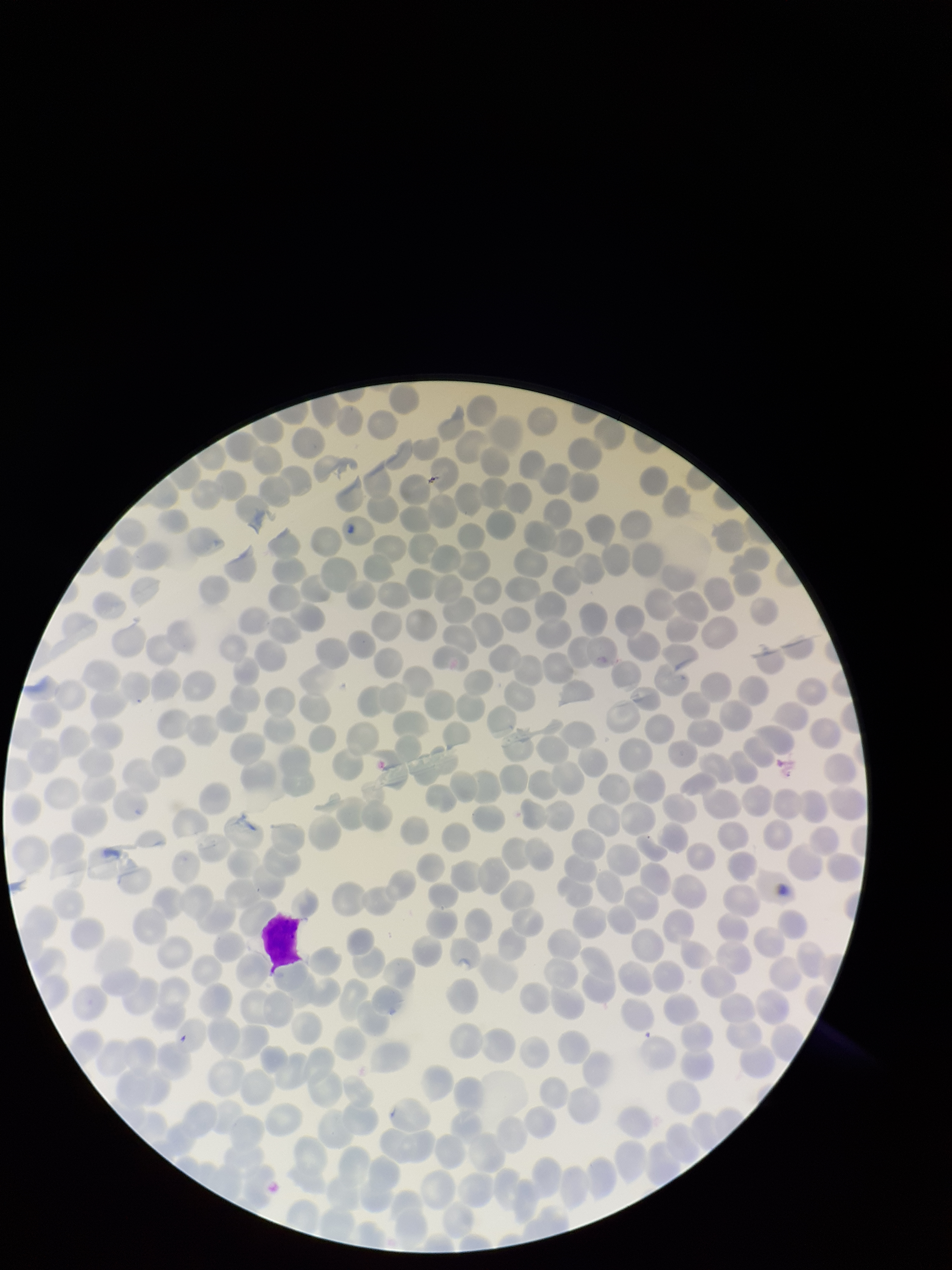

Stained with Giemsa. Preparation: thin smear. Parasitized red blood cells: none seen. Photographed through the microscope eyepiece with a smartphone camera. Red blood cell count: 225. Image is 952×1270 pixels. Patient malaria status: positive. Parasitized red blood cell count: 0. Species reported for this patient: Plasmodium falciparum. One field from this slide.